Give the extent of all Plasmodium falciparum-infected red blood cells.
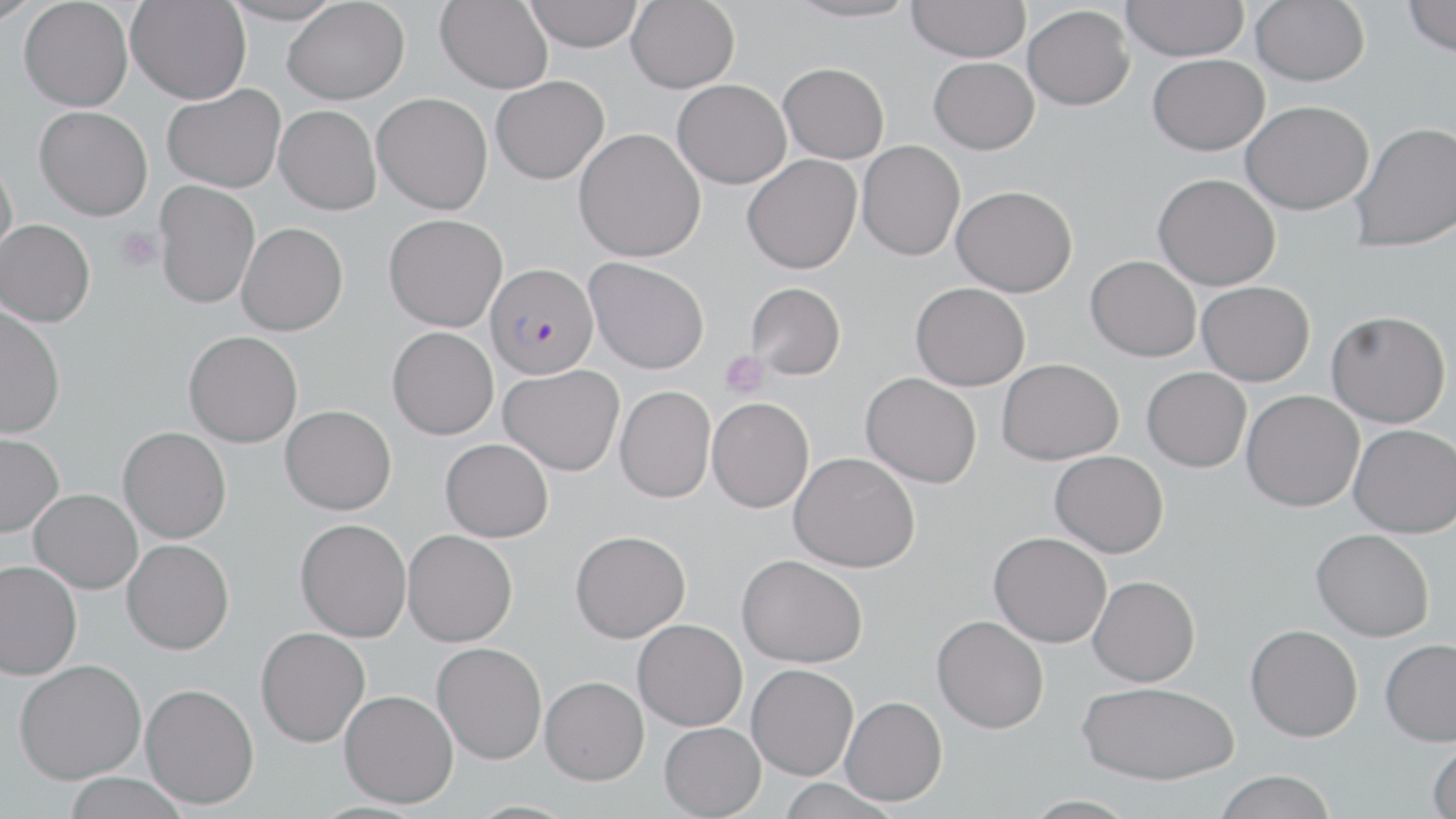
Approximate bounding boxes as (x1,y1)-(x2,y2) corner pairs in pixels.
Plasmodium falciparum-infected red blood cells: (485,262)-(599,379).

slide-level diagnosis = Plasmodium falciparum
stain = May-Grünwald-Giemsa
platelet locations = approximate bounding boxes as (x1,y1)-(x2,y2) corner pairs in pixels: (115,227)-(163,272), (720,351)-(769,397)
uninfected red blood cell locations = approximate bounding boxes as (x1,y1)-(x2,y2) corner pairs in pixels: (0,0)-(43,26), (19,0)-(133,111), (126,0)-(251,104), (222,0)-(346,26), (435,0)-(553,93), (523,0)-(644,52), (627,0)-(739,93), (784,0)-(922,23), (1120,0)-(1249,61), (1250,0)-(1369,86), (1402,0)-(1456,58), (282,1)-(410,104), (907,1)-(1031,62), (1023,5)-(1135,110), (1147,53)-(1269,155), (928,57)-(1039,154), (779,62)-(889,162), (491,76)-(609,184), (673,79)-(791,188), (162,84)-(286,193), (372,93)-(492,214), (1241,100)-(1374,215), (274,104)-(381,215), (35,106)-(153,220), (1350,121)-(1455,252), (575,128)-(706,262), (857,141)-(965,261), (742,154)-(862,274), (0,157)-(18,266), (1153,173)-(1280,290), (154,179)-(260,309), (952,184)-(1077,297), (384,214)-(507,331), (0,219)-(95,326), (236,222)-(348,335), (1086,255)-(1201,361), (584,257)-(710,374), (1197,281)-(1315,386), (745,282)-(846,380), (911,282)-(1031,390), (0,305)-(66,439), (1326,310)-(1451,428), (387,326)-(498,440), (184,330)-(303,447), (997,358)-(1124,464), (499,364)-(624,476), (1142,367)-(1251,472), (861,372)-(982,488), (615,385)-(715,503), (1241,390)-(1364,512), (707,397)-(814,513), (280,404)-(397,515), (1348,423)-(1456,537), (118,426)-(231,543), (0,432)-(63,537), (441,438)-(554,541), (1050,450)-(1169,557), (789,452)-(920,572), (29,488)-(143,593), (295,517)-(412,642), (1311,528)-(1434,641), (403,530)-(517,646), (570,530)-(691,642), (989,531)-(1112,647), (122,539)-(234,654), (737,554)-(868,667), (0,560)-(82,679), (1088,575)-(1200,686), (931,615)-(1049,734), (633,619)-(748,731), (1245,624)-(1363,741), (256,627)-(371,747), (1380,638)-(1456,746), (432,642)-(547,764), (13,659)-(147,784), (746,664)-(858,780), (540,675)-(649,784), (1078,681)-(1240,784), (140,683)-(259,809), (339,689)-(459,808), (841,695)-(947,806), (659,722)-(766,818), (1427,740)-(1456,818), (1214,770)-(1337,819), (61,772)-(191,819), (775,779)-(901,818), (1018,794)-(1144,819)
image size = 1456×819 pixels
magnification = 1000x
preparation = thin blood film
field of view = one of a larger specimen
modality = light microscopy